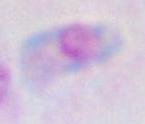

Summary:
  - Identification: Toxoplasma gondii
  - Magnification: 1000x
  - Modality: micrograph